Report the malaria status of this cell.
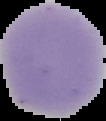

It is uninfected.

image type = cell region segmented out of the field of view; surrounding area masked to black
image size = 106×121 pixels
preparation = thin blood film